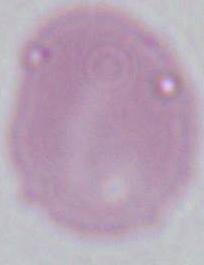

1000x magnification. Micrograph. A red blood cell is seen.